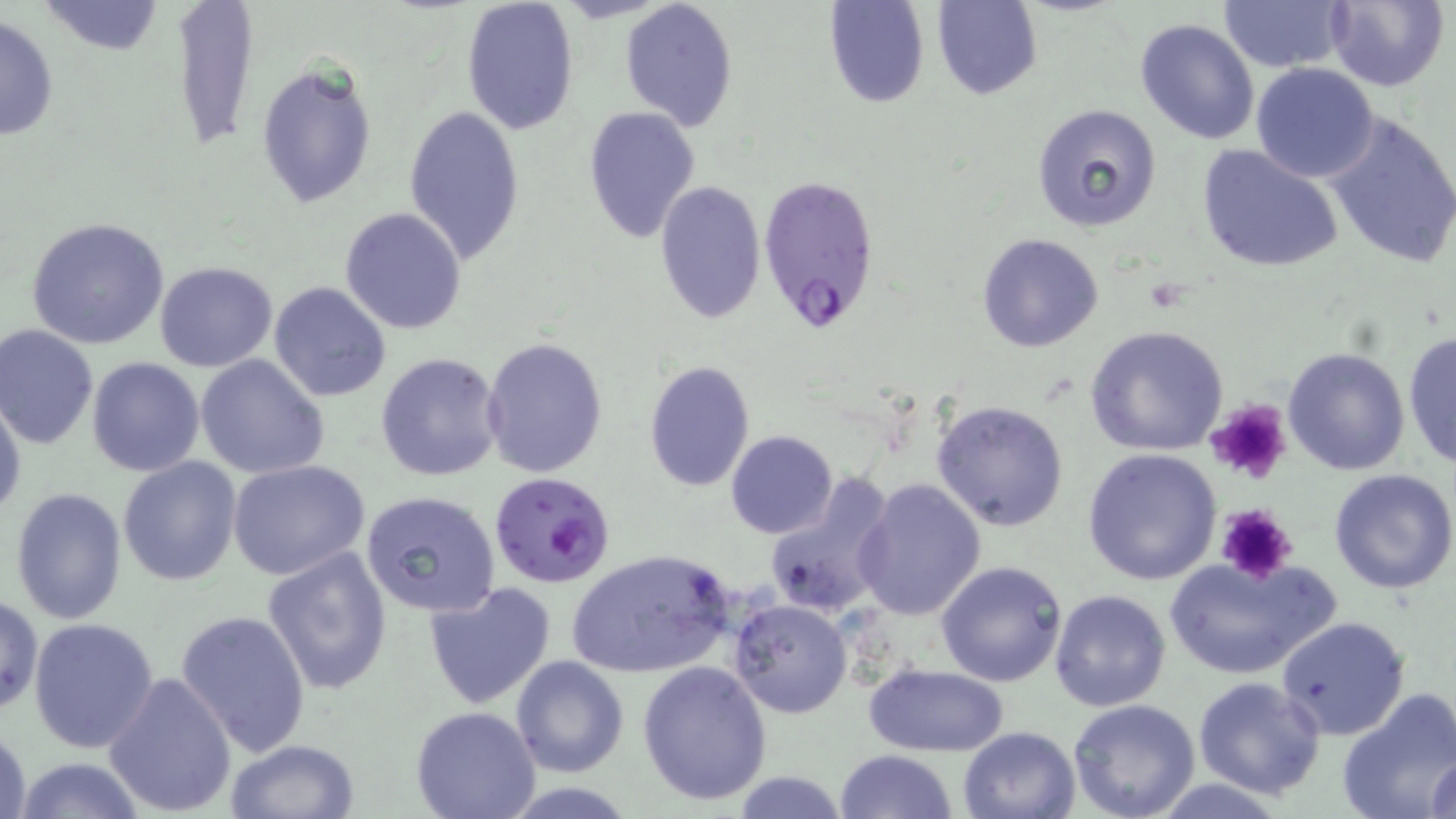

slide-level diagnosis = Plasmodium falciparum
preparation = thin blood smear
stain = May-Grünwald-Giemsa
uninfected red blood cell locations = approximate bounding boxes as [x1, y1, x2, y2] in pixels: [165, 0, 260, 154], [825, 0, 930, 109], [934, 0, 1042, 100], [1324, 0, 1449, 91], [38, 1, 166, 55], [461, 1, 580, 137], [620, 1, 739, 131], [1218, 1, 1349, 74], [0, 14, 59, 141], [1134, 17, 1261, 146], [256, 61, 378, 211], [1251, 63, 1382, 183], [1031, 103, 1164, 231], [403, 104, 525, 265], [583, 108, 701, 244], [1321, 110, 1456, 269], [1196, 143, 1345, 274], [653, 179, 767, 328], [339, 207, 468, 335], [25, 217, 170, 352], [977, 232, 1105, 353], [153, 261, 278, 371], [268, 281, 394, 403], [0, 324, 98, 449], [1084, 324, 1230, 458], [1402, 330, 1456, 471], [480, 336, 608, 477], [1283, 345, 1411, 476], [375, 352, 505, 483], [194, 353, 330, 480], [86, 357, 206, 477], [642, 360, 755, 492], [0, 391, 25, 526], [932, 399, 1069, 532], [726, 430, 838, 539], [1082, 447, 1222, 586], [118, 456, 242, 587], [228, 460, 372, 582], [1329, 467, 1456, 594], [763, 473, 899, 620], [855, 478, 987, 622], [9, 486, 128, 627], [360, 490, 501, 620], [263, 547, 393, 696], [565, 548, 738, 679], [1165, 554, 1332, 681], [937, 559, 1068, 686], [424, 581, 558, 711], [1049, 589, 1173, 713], [0, 595, 43, 718], [729, 598, 852, 718], [176, 609, 311, 758], [1276, 615, 1409, 740], [29, 617, 160, 754], [510, 655, 629, 776], [637, 659, 772, 805], [865, 663, 1009, 756], [104, 671, 237, 817], [1192, 676, 1327, 802], [1337, 688, 1456, 819], [1068, 699, 1200, 819], [411, 706, 541, 819], [0, 722, 31, 819], [957, 725, 1082, 818], [224, 738, 363, 819], [835, 749, 958, 819], [1426, 750, 1456, 819], [12, 757, 148, 817], [731, 773, 850, 817]
magnification = 1000x
image size = 1456×819 pixels
field of view = single
Plasmodium falciparum-infected red blood cell locations = approximate bounding boxes as [x1, y1, x2, y2] in pixels: [759, 172, 881, 339], [489, 471, 616, 589]
modality = light microscopy
platelet locations = approximate bounding boxes as [x1, y1, x2, y2] in pixels: [1201, 399, 1293, 486], [1213, 503, 1298, 585]